Name the parasite shown.
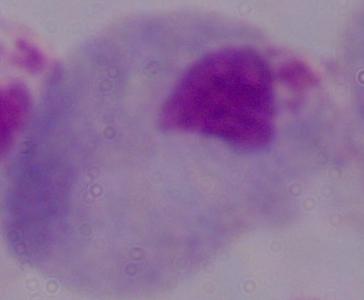
A trichomonad.

Summary:
  - Magnification: 1000x
  - Modality: photomicrograph